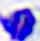

Summary:
  - Magnification: 400x
  - Identification: leukocyte
  - Modality: photomicrograph